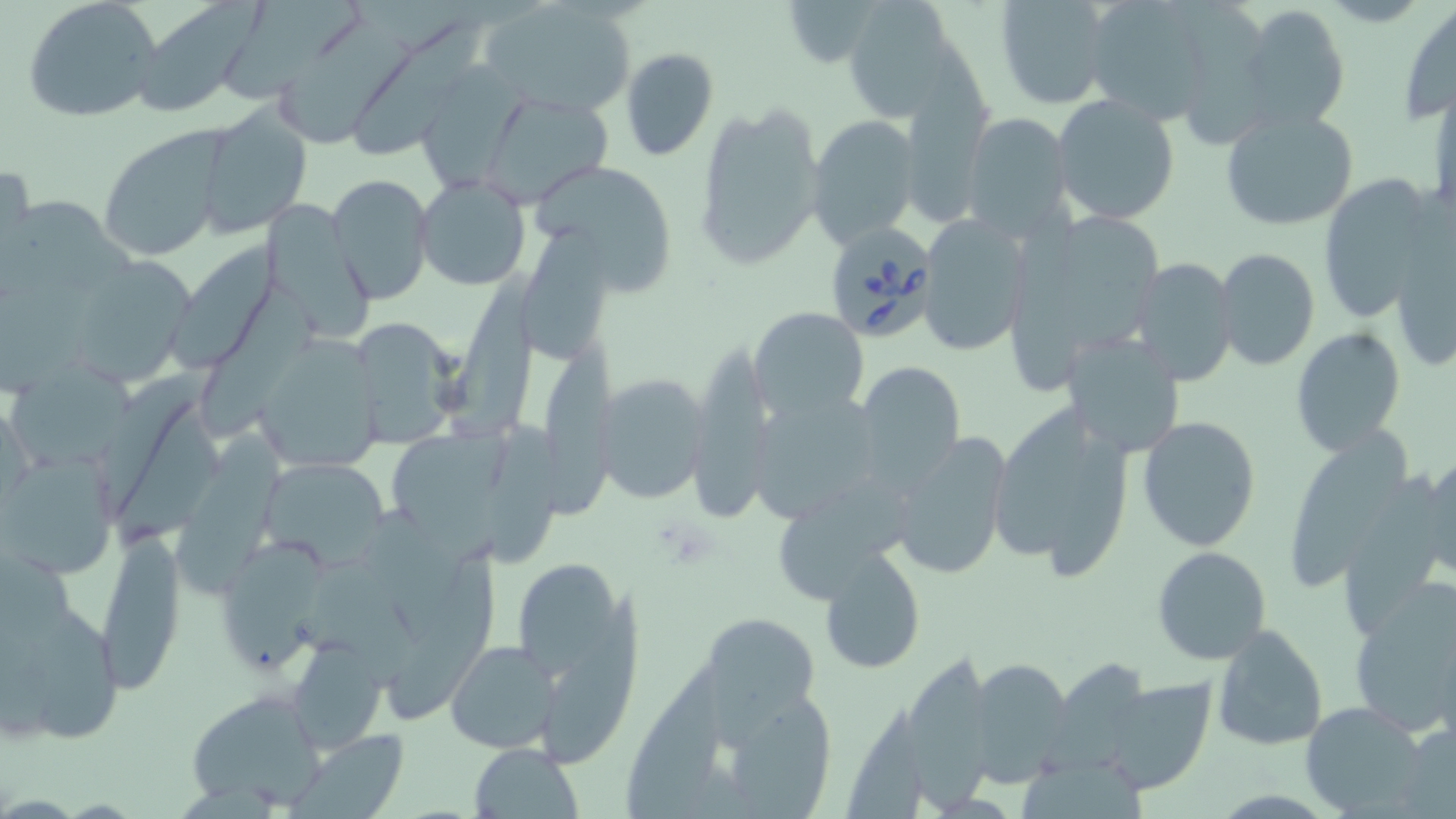 Approximate bounding boxes as (x1, y1, x2, y2) in pixels. Uninfected red blood cell locations: (132, 0, 265, 114), (480, 0, 637, 119), (782, 0, 882, 71), (840, 0, 969, 125), (991, 0, 1116, 111), (1081, 0, 1216, 123), (22, 1, 161, 123), (1398, 1, 1456, 127), (220, 3, 360, 108), (1237, 3, 1350, 134), (277, 20, 416, 153), (356, 23, 491, 160), (620, 47, 719, 161), (905, 50, 997, 230), (411, 61, 530, 192), (1430, 82, 1456, 224), (476, 91, 614, 208), (1053, 93, 1180, 226), (693, 101, 827, 271), (192, 105, 313, 240), (1219, 107, 1359, 231), (960, 111, 1074, 241), (806, 114, 919, 248), (98, 128, 229, 260), (530, 160, 679, 291), (1, 163, 35, 263), (326, 173, 434, 306), (1317, 174, 1446, 323), (414, 175, 530, 292), (994, 206, 1170, 394), (916, 214, 1032, 357), (1387, 221, 1456, 374), (519, 223, 618, 368), (173, 245, 277, 377), (1216, 248, 1320, 371), (1129, 256, 1239, 386), (76, 258, 194, 389), (451, 260, 538, 444), (195, 288, 318, 445), (750, 306, 869, 418), (350, 316, 468, 447), (1289, 326, 1407, 455), (1060, 330, 1187, 459), (255, 334, 385, 475), (689, 341, 776, 517), (548, 354, 618, 526), (13, 359, 137, 474), (853, 360, 967, 491), (593, 372, 711, 505), (98, 375, 209, 516), (751, 393, 884, 524), (988, 401, 1138, 578), (108, 407, 237, 558), (1136, 415, 1263, 552), (487, 419, 575, 569), (1289, 423, 1409, 594), (381, 425, 511, 557), (174, 431, 285, 597), (889, 431, 1013, 582), (1, 451, 117, 581), (258, 456, 391, 567), (1410, 456, 1456, 587), (95, 531, 187, 694), (220, 536, 325, 678), (506, 545, 647, 759), (1152, 546, 1272, 664), (386, 550, 500, 727), (816, 550, 927, 674), (1346, 578, 1456, 741), (0, 600, 122, 743), (700, 613, 821, 727), (1210, 624, 1328, 752), (285, 635, 389, 755), (445, 640, 561, 755), (966, 656, 1074, 783), (1051, 658, 1152, 771), (908, 661, 990, 813), (617, 662, 726, 812), (1101, 679, 1215, 796), (185, 688, 329, 812), (713, 691, 835, 817), (1302, 702, 1433, 817), (1393, 724, 1456, 817), (289, 730, 411, 818), (469, 743, 584, 819). Babesia divergens-infected red blood cell locations: (821, 222, 939, 344). Slide-level diagnosis: Babesia divergens. Light microscopy. May-Grünwald-Giemsa stain. Image is 1456×819 pixels. Single field of view. Thin blood smear. Captured at 1000x magnification.